Point out each malaria parasite.
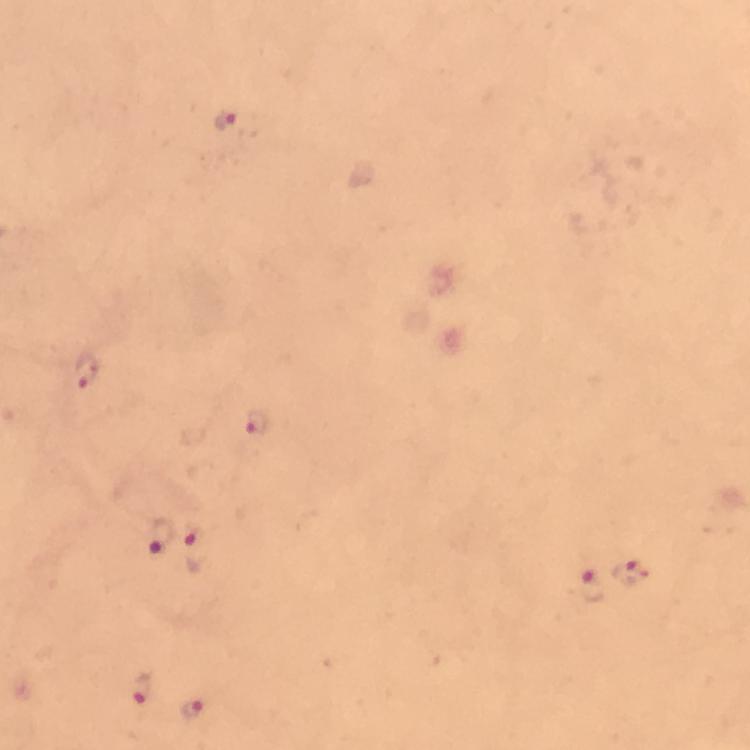

Approximate object centers, in pixels from the top-left corner.
Malaria parasites: (x=228, y=118), (x=86, y=370), (x=257, y=420), (x=161, y=534), (x=198, y=548), (x=631, y=572), (x=592, y=584), (x=144, y=692), (x=193, y=713).

immersion oil = used
capture = smartphone camera through the microscope
cropped from = one field of view
preparation = thick blood smear
magnification = 100x
context = from a malaria diagnostic workup
stain = Giemsa
image size = 750×750 pixels